Report the malaria status of this cell.
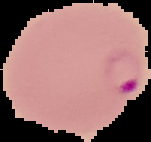
It is parasitized.

{
  "preparation": "thin blood film",
  "image_type": "segmented cell region with the area outside set to black",
  "image_size": "151×142 pixels"
}